Assess this cell for malaria.
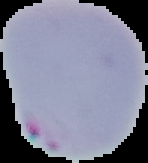
Parasitized.

Summary:
  - Preparation: thin blood smear
  - Image type: segmented cell region with the area outside set to black
  - Image size: 148×163 pixels